Report the malaria status of this cell.
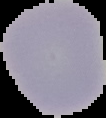

Uninfected.

Summary:
  - Preparation: thin blood smear
  - Image type: segmented cell region on a black background
  - Image size: 106×118 pixels